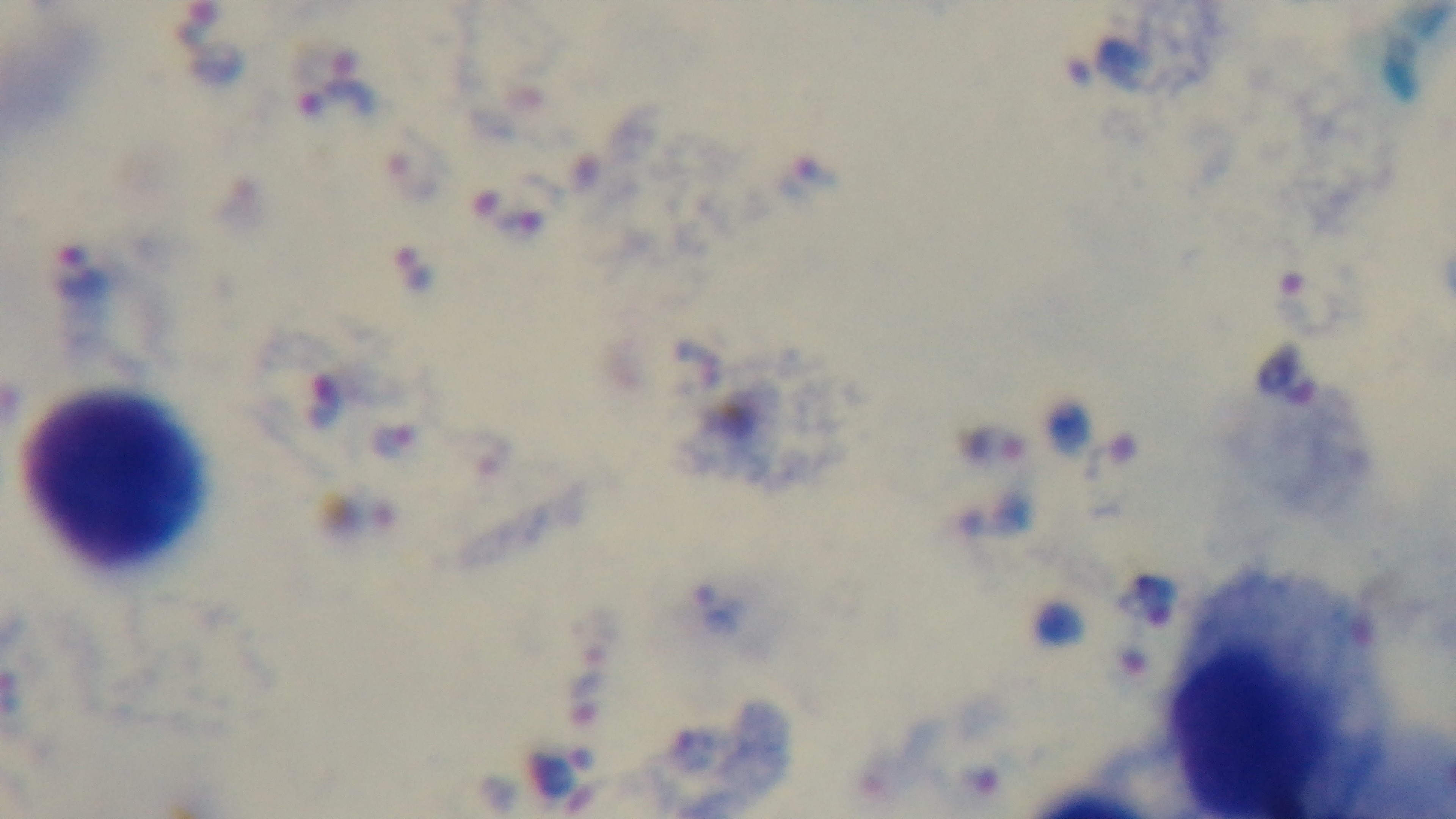

{
  "field_of_view": "one from the slide",
  "capture": "mounted 4K digital camera",
  "preparation": "thick",
  "modality": "light microscopy",
  "objective": "100x oil immersion",
  "stain": "Giemsa",
  "malaria_status": "positive"
}